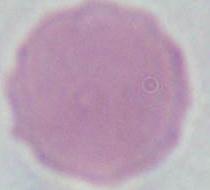

identification = red blood cell
magnification = 1000x
modality = photomicrograph